Report the malaria status of this cell.
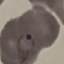

Parasitized.

preparation = thin smear
image type = automatically extracted cell patch, resized to 64 × 64 pixels
stain = Giemsa
capture = smartphone camera at the microscope eyepiece